Locate and identify every blood parasite.
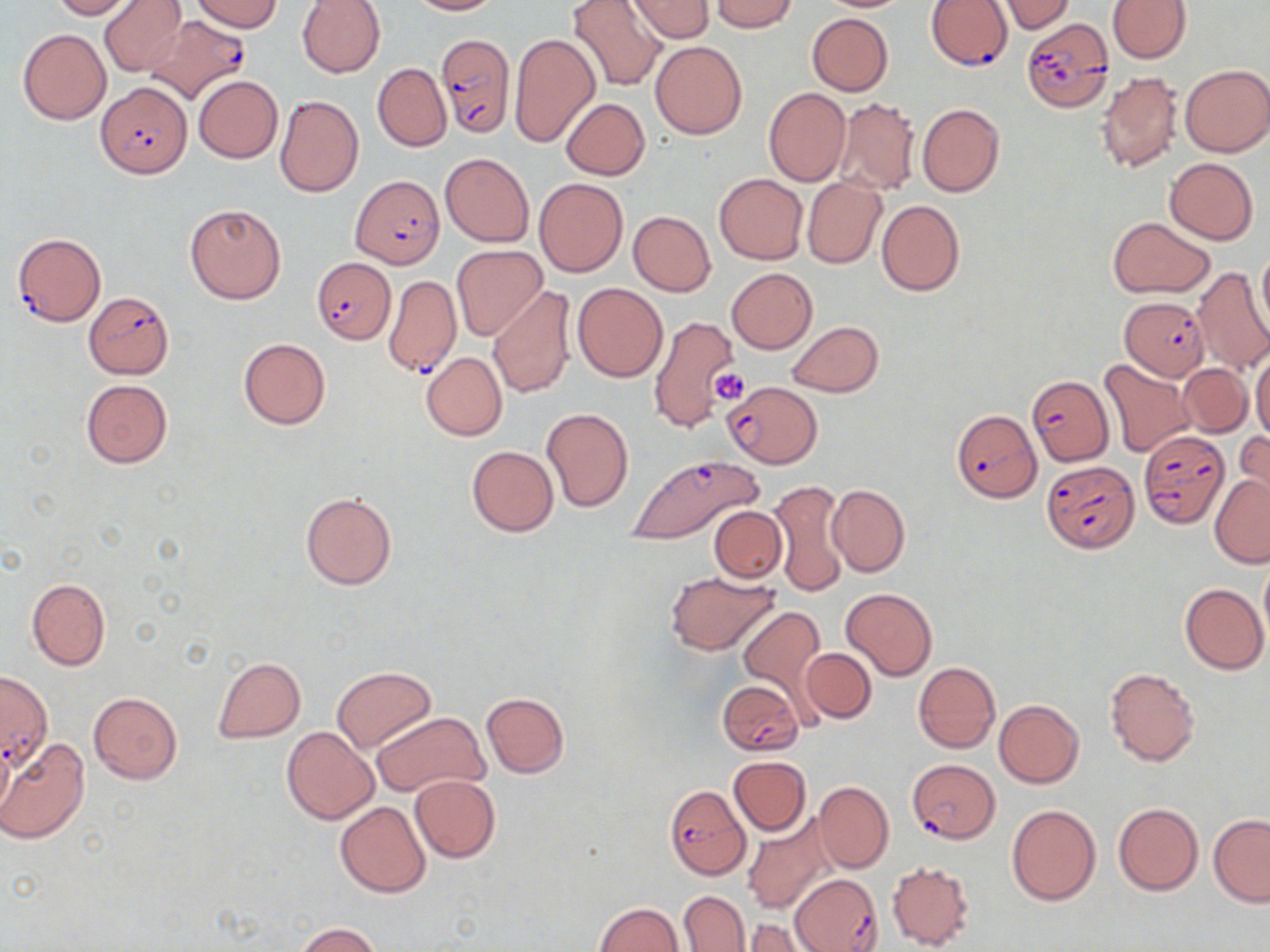
Approximate bounding boxes as (x1,y1)-(x2,y2) corner pairs in pixels.
Plasmodium falciparum-infected red blood cells: (925,1)-(1012,70), (145,15)-(251,105), (1022,17)-(1114,113), (436,34)-(516,138), (96,82)-(191,178), (349,175)-(443,269), (11,233)-(106,326), (313,259)-(396,343), (384,275)-(461,377), (84,292)-(173,378), (1119,297)-(1210,381), (1028,377)-(1111,467), (723,382)-(821,466), (952,408)-(1042,502), (1139,429)-(1228,527), (624,453)-(766,547), (1044,459)-(1138,553), (0,669)-(53,773), (716,677)-(805,756), (907,757)-(999,842), (664,785)-(751,878), (790,874)-(881,951).
No Plasmodium ovale, Plasmodium malariae, Plasmodium vivax, Babesia divergens, or Trypanosoma brucei observed.

{
  "slide_level_diagnosis": "Plasmodium falciparum",
  "preparation": "thin blood smear",
  "stain": "May-Grünwald-Giemsa",
  "modality": "light microscopy",
  "field_of_view": "one of a larger specimen",
  "image_size": "1270×952 pixels",
  "uninfected_red_blood_cell_locations": "approximate bounding boxes as (x1,y1)-(x2,y2) corner pairs in pixels: (49,0)-(133,20), (100,0)-(187,76), (191,0)-(283,33), (296,0)-(385,78), (405,0)-(499,15), (567,0)-(667,93), (627,0)-(713,41), (815,0)-(916,12), (1106,0)-(1191,63), (707,1)-(801,32), (997,1)-(1075,34), (806,12)-(893,96), (17,28)-(111,124), (508,32)-(600,149), (650,42)-(747,140), (372,63)-(451,152), (1180,64)-(1269,156), (1097,72)-(1183,173), (193,74)-(282,163), (764,88)-(850,186), (274,95)-(364,197), (561,97)-(649,179), (836,97)-(919,195), (917,103)-(1004,197), (439,151)-(534,247), (1165,157)-(1258,245), (713,173)-(808,264), (534,177)-(628,277), (802,177)-(885,268), (877,200)-(965,296), (185,203)-(285,303), (628,211)-(715,296), (1108,217)-(1215,297), (451,244)-(548,341), (1256,244)-(1270,342), (1191,266)-(1270,376), (727,268)-(817,353), (572,282)-(668,382), (488,285)-(577,398), (607,292)-(719,411), (647,314)-(742,431), (786,321)-(884,397), (237,338)-(331,430), (1250,348)-(1269,441), (421,353)-(507,440), (1099,358)-(1194,457), (1179,363)-(1253,437), (80,379)-(173,469), (541,407)-(633,513), (1234,432)-(1269,511), (466,445)-(558,536), (1210,473)-(1270,567), (769,479)-(848,599), (827,483)-(910,577), (300,492)-(397,590), (709,506)-(786,582), (694,510)-(787,642), (1258,558)-(1270,650), (665,571)-(779,655), (27,578)-(110,669), (1179,583)-(1269,675), (840,587)-(938,680), (738,607)-(823,697), (800,647)-(876,724), (212,656)-(305,743), (913,661)-(1000,754), (331,666)-(436,754), (1104,666)-(1200,767), (88,690)-(182,784), (480,692)-(569,777), (993,699)-(1084,788), (372,711)-(489,800), (282,726)-(379,825), (0,736)-(12,814), (1,739)-(89,844), (729,755)-(810,835), (409,775)-(500,862), (813,782)-(893,874), (335,801)-(431,898), (1112,802)-(1204,895), (1006,803)-(1102,905), (741,813)-(837,916), (1208,814)-(1270,907), (886,860)-(974,950), (679,890)-(749,951), (595,903)-(685,951), (740,918)-(818,951), (296,923)-(380,952)",
  "platelet_locations": "approximate bounding boxes as (x1,y1)-(x2,y2) corner pairs in pixels: (708,368)-(753,406)",
  "magnification": "1000x"
}